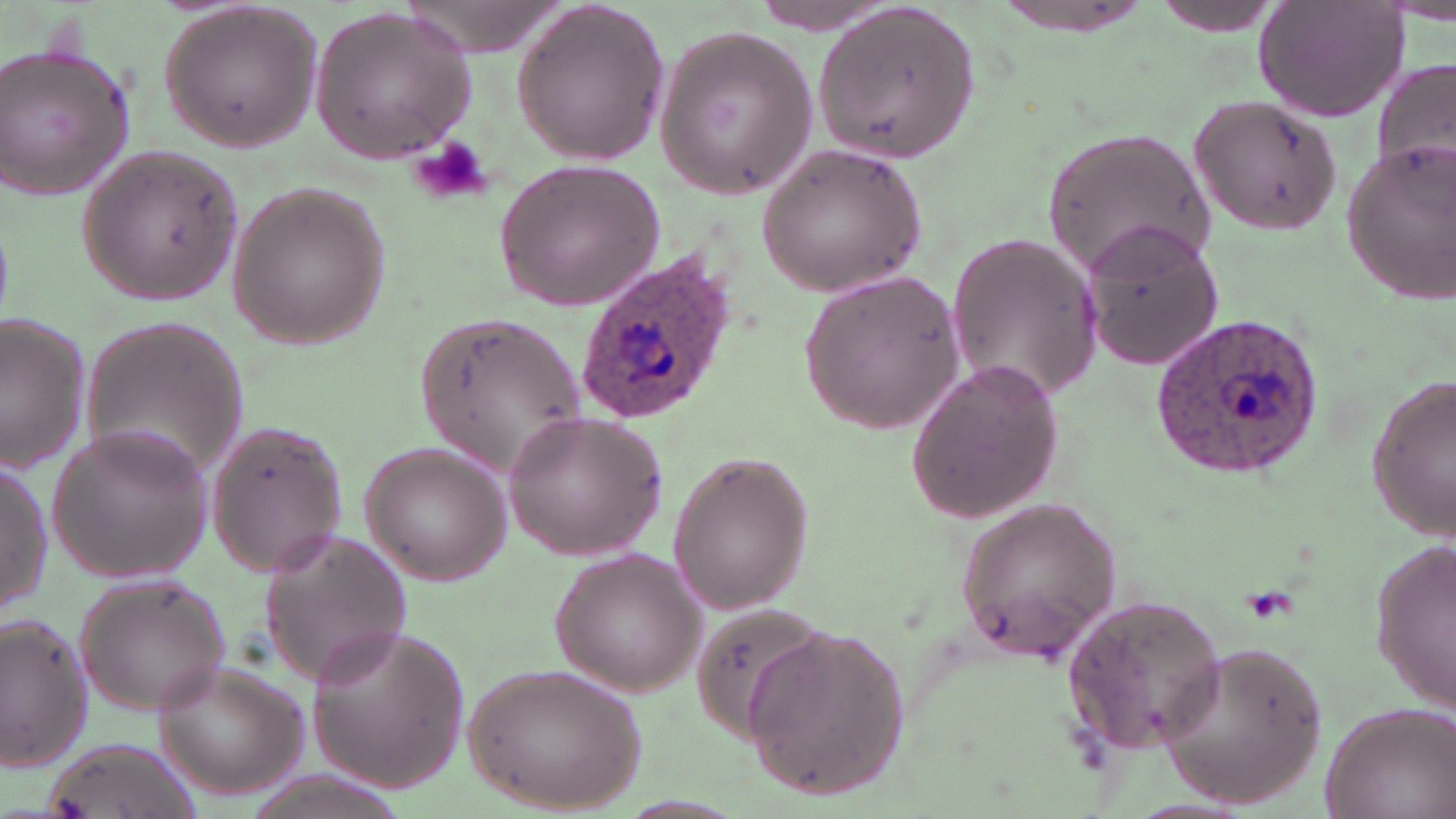 Approximate bounding boxes as [x1, y1, x2, y2] in pixels. Uninfected red blood cell locations: [509, 0, 672, 166], [1150, 1, 1291, 36], [1254, 1, 1410, 122], [746, 2, 900, 37], [992, 3, 1152, 36], [158, 4, 322, 151], [812, 4, 981, 161], [308, 6, 478, 164], [652, 24, 823, 197], [0, 40, 138, 203], [1373, 57, 1454, 187], [1188, 95, 1344, 236], [1043, 126, 1215, 280], [1337, 136, 1455, 303], [756, 140, 931, 298], [78, 143, 242, 301], [493, 157, 666, 313], [227, 180, 387, 351], [1078, 222, 1227, 374], [944, 231, 1104, 404], [795, 268, 969, 437], [413, 311, 585, 476], [79, 312, 247, 484], [1, 315, 92, 470], [905, 357, 1065, 525], [1365, 379, 1456, 537], [502, 409, 668, 562], [203, 414, 351, 578], [46, 421, 214, 586], [357, 443, 512, 585], [665, 453, 814, 615], [0, 459, 52, 617], [952, 498, 1122, 664], [256, 528, 412, 688], [1371, 538, 1456, 710], [551, 547, 707, 695], [73, 571, 233, 715], [1060, 594, 1229, 756], [0, 614, 95, 773], [305, 622, 472, 793], [741, 626, 913, 801], [1154, 641, 1328, 810], [153, 659, 306, 798], [465, 662, 646, 815], [1319, 700, 1454, 819], [39, 734, 199, 819]. Platelet locations: [408, 135, 492, 205]. Plasmodium ovale-infected red blood cell locations: [575, 251, 740, 422], [1150, 314, 1326, 480]. Slide-level diagnosis: Plasmodium ovale. Optical microscopy. Image is 1456×819 pixels. One field of a larger specimen. Captured at 1000x magnification. Thin blood film. May-Grünwald-Giemsa stain.